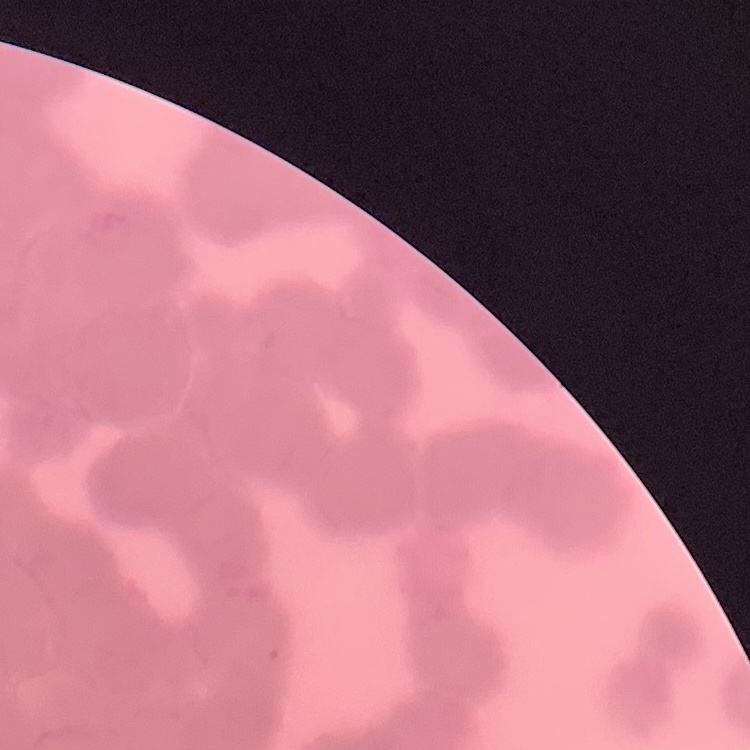
erythrocyte_morphology: rouleaux formation
image_type: square crop of a larger photomicrograph
preparation: thin blood film
stain: Field's or Giemsa